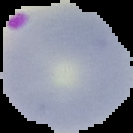
Result: malaria parasites detected. Segmented cell region on a black background. From a thin blood smear. Image is 133×133 pixels.